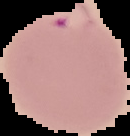
result = Plasmodium parasites detected
image size = 130×136 pixels
image type = segmented cell region on a black background
preparation = thin blood film